Assess this cell for malaria.
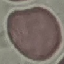
It is uninfected.

capture = smartphone camera at the microscope eyepiece
stain = Giemsa
image type = cell patch, automatically extracted from a larger field of view and resized to 64 × 64 pixels
preparation = thin smear